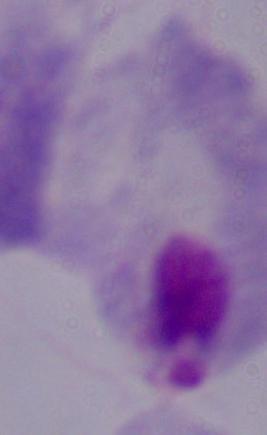
identification = trichomonad
modality = micrograph
magnification = 1000x